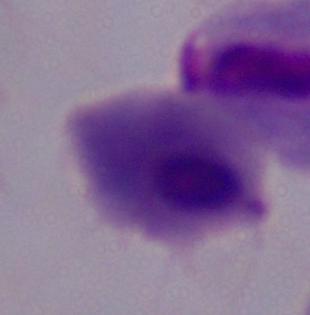

Summary:
  - Modality: micrograph
  - Magnification: 1000x
  - Identification: trichomonad